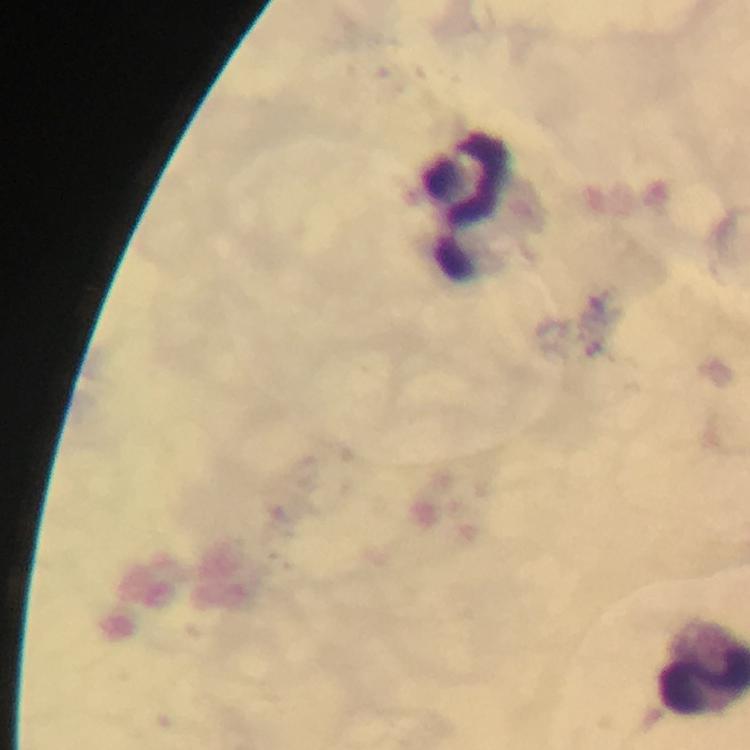

immersion oil = used
capture = smartphone camera through the microscope
leukocyte locations = approximate centers as {x, y} in pixels: {467, 206}
cropped from = one field of view
preparation = thick smear
image size = 750×750 pixels
magnification = 100x
context = from a diagnostic examination for malaria
stain = Giemsa
Plasmodium parasites = none seen